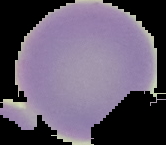
Image is 166×145 pixels. From a thin blood smear. Cell region segmented out of the field of view; the surrounding area is masked to black. Malaria status: uninfected.